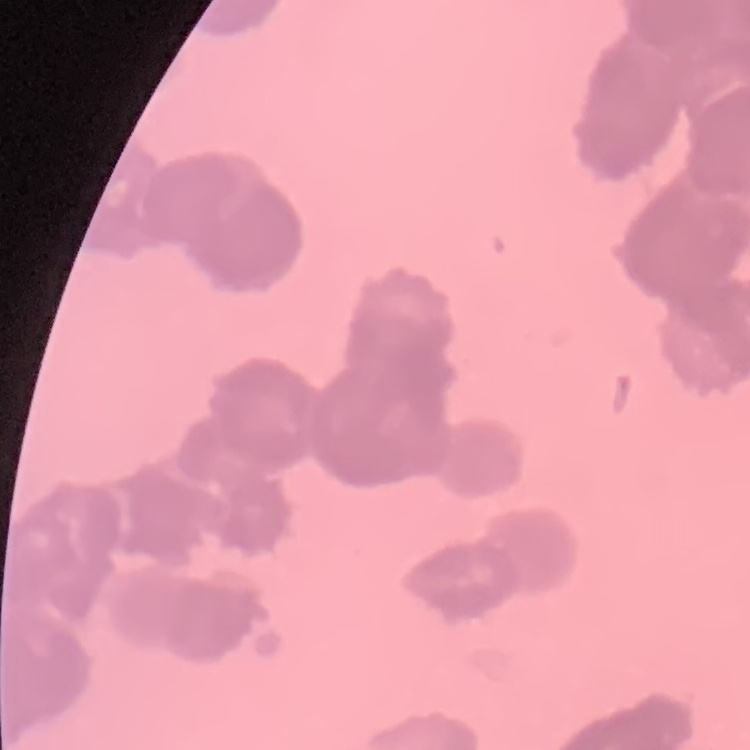

Summary:
  - Red blood cell morphology: rouleaux formation
  - Stain: Field's or Giemsa
  - Preparation: thin blood film
  - Image type: square crop of a larger photomicrograph